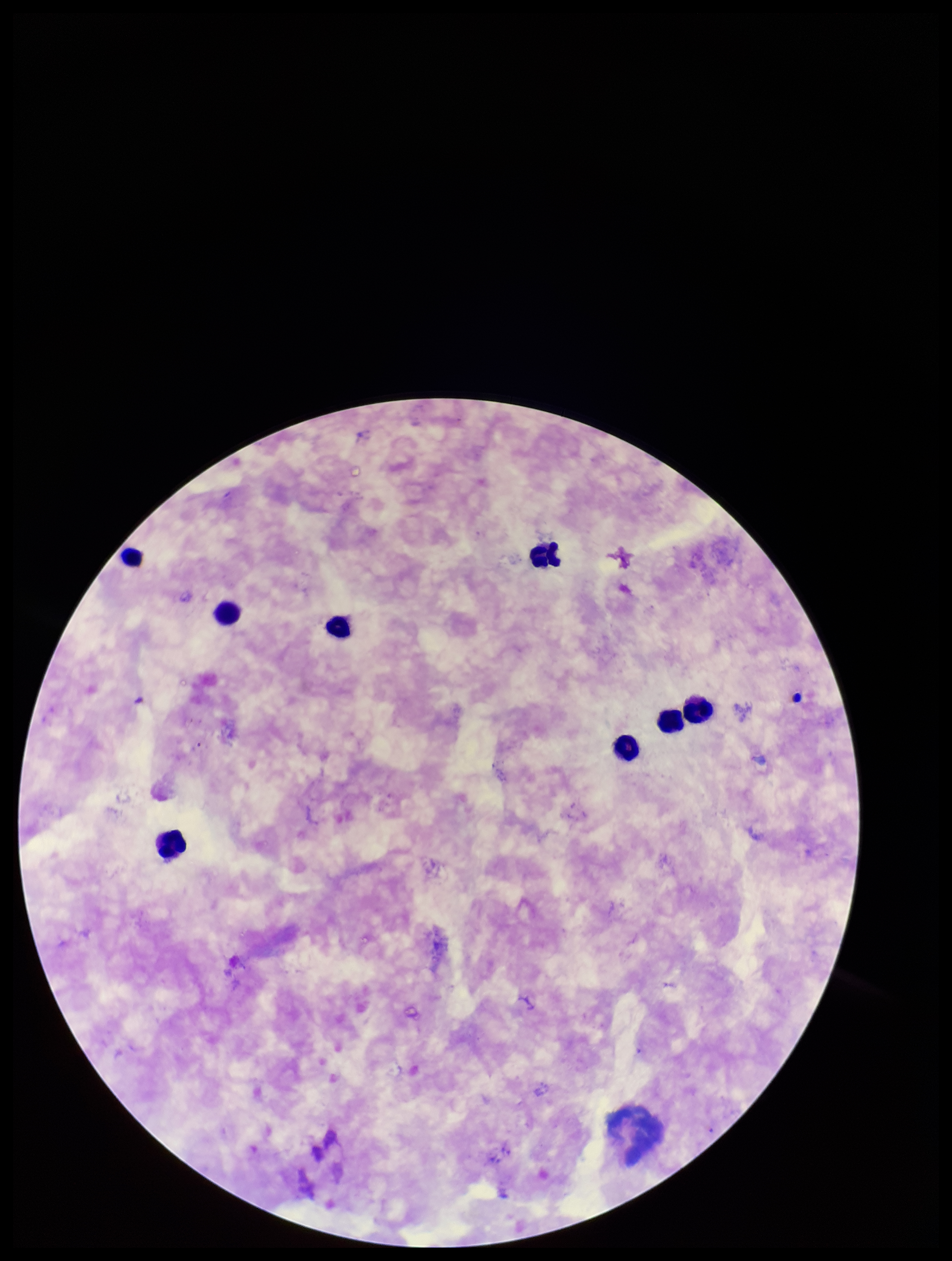
{
  "capture": "smartphone photograph through the microscope eyepiece",
  "parasite_count": 0,
  "image_size": "952×1261 pixels",
  "leukocyte_count": 8,
  "preparation": "thick blood smear",
  "field_of_view": "one from this slide",
  "stain": "Giemsa",
  "plasmodium_parasites": "none seen",
  "patient_malaria_status": "negative"
}